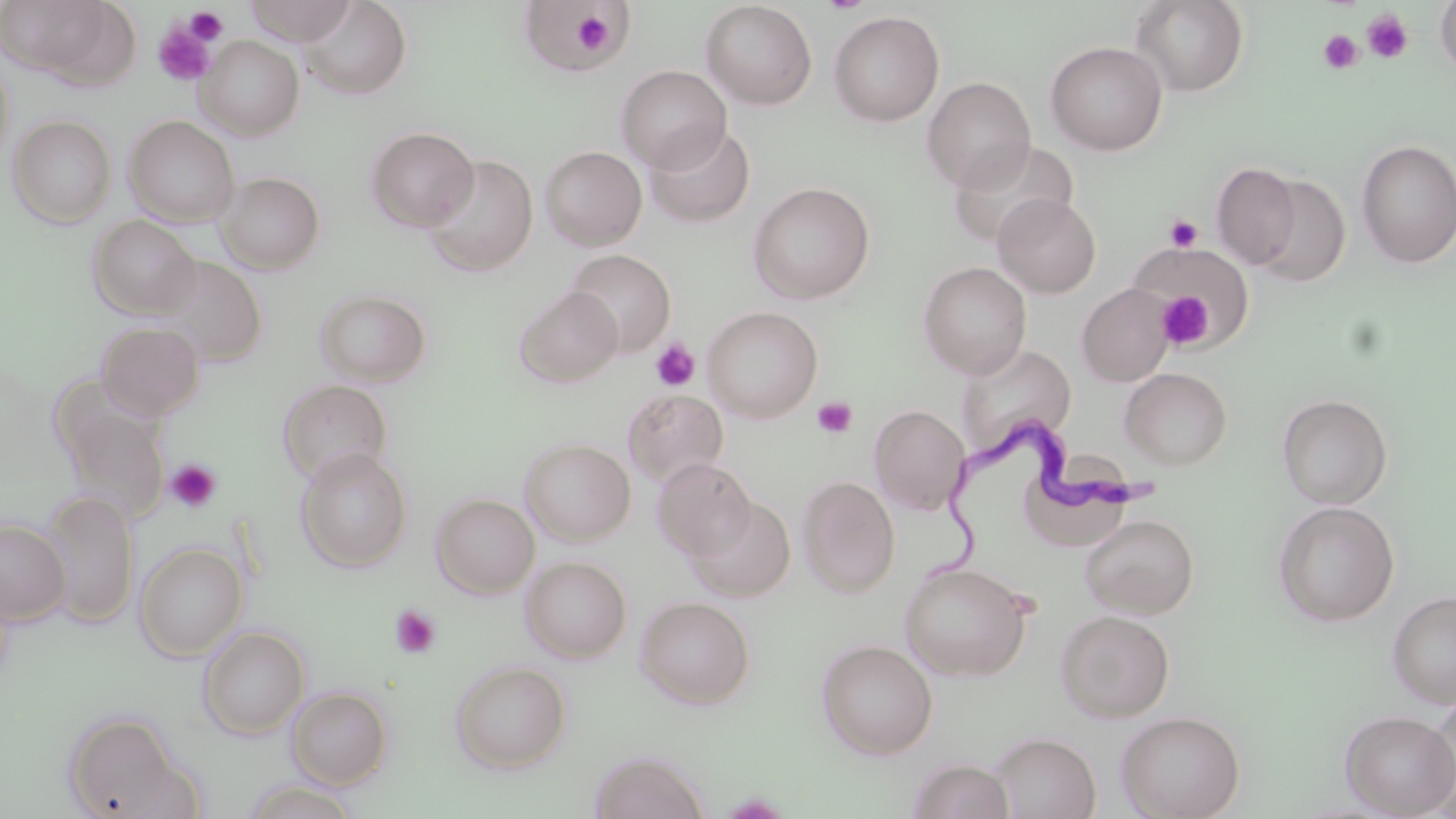
slide-level diagnosis = Trypanosoma brucei
platelet locations = approximate bounding boxes as (x1, y1, x2, y2) in pixels: (185, 7, 228, 46), (569, 7, 626, 60), (1362, 9, 1414, 63), (152, 19, 219, 86), (1318, 29, 1364, 75), (1164, 214, 1203, 253), (1155, 291, 1214, 349), (650, 338, 701, 392), (812, 396, 857, 440), (164, 459, 221, 514), (389, 604, 441, 658)
image size = 1456×819 pixels
modality = optical microscopy
Trypanosoma brucei locations = approximate bounding boxes as (x1, y1, x2, y2) in pixels: (926, 419, 1166, 582)
uninfected red blood cell locations = approximate bounding boxes as (x1, y1, x2, y2) in pixels: (245, 0, 358, 45), (1129, 0, 1250, 97), (1434, 0, 1456, 82), (301, 1, 412, 99), (701, 1, 817, 109), (40, 3, 146, 96), (517, 3, 628, 75), (828, 10, 945, 126), (195, 36, 304, 141), (1045, 41, 1168, 155), (0, 55, 14, 168), (615, 65, 732, 172), (922, 76, 1036, 192), (8, 115, 116, 228), (123, 115, 239, 226), (644, 122, 756, 229), (366, 127, 479, 232), (1356, 138, 1456, 269), (947, 139, 1079, 249), (540, 146, 647, 250), (423, 154, 538, 276), (1211, 161, 1302, 269), (217, 172, 325, 274), (1249, 174, 1351, 288), (748, 181, 875, 304), (993, 193, 1101, 297), (87, 215, 200, 318), (1127, 247, 1255, 347), (564, 249, 676, 356), (152, 255, 269, 368), (918, 261, 1032, 378), (1077, 283, 1174, 387), (515, 286, 623, 388), (314, 288, 432, 387), (702, 306, 823, 423), (96, 321, 204, 420), (954, 342, 1077, 459), (1120, 367, 1233, 470), (277, 379, 393, 486), (623, 389, 728, 487), (1277, 393, 1392, 508), (57, 397, 170, 525), (870, 405, 970, 516), (519, 438, 635, 546), (295, 448, 412, 572), (652, 458, 756, 561), (797, 476, 899, 597), (38, 491, 138, 627), (431, 493, 539, 598), (688, 497, 796, 602), (1273, 500, 1400, 627), (1080, 514, 1199, 618), (0, 519, 70, 625), (135, 542, 248, 661), (520, 556, 632, 662), (898, 561, 1033, 681), (1387, 589, 1456, 707), (635, 596, 756, 709), (1055, 609, 1175, 723), (197, 627, 309, 739), (816, 639, 938, 759), (450, 661, 571, 774), (286, 687, 392, 789), (1423, 695, 1456, 811), (1116, 710, 1246, 819), (1340, 710, 1456, 817), (62, 712, 186, 818), (989, 732, 1100, 819), (590, 750, 711, 819), (908, 758, 1015, 819), (243, 779, 360, 818)
preparation = thin blood smear
magnification = 1000x
stain = May-Grünwald-Giemsa
field of view = one of a larger specimen